Report the malaria status of this cell.
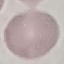
Uninfected.

Thin blood film. Automatically extracted cell patch, resized to 64 × 64 pixels. Acquired by smartphone through the microscope eyepiece. Giemsa-stained preparation.